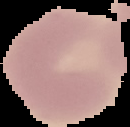
From a thin blood smear. Image is 130×127 pixels. Malaria status: uninfected. Cell region segmented out of the field of view; the surrounding area is masked to black.